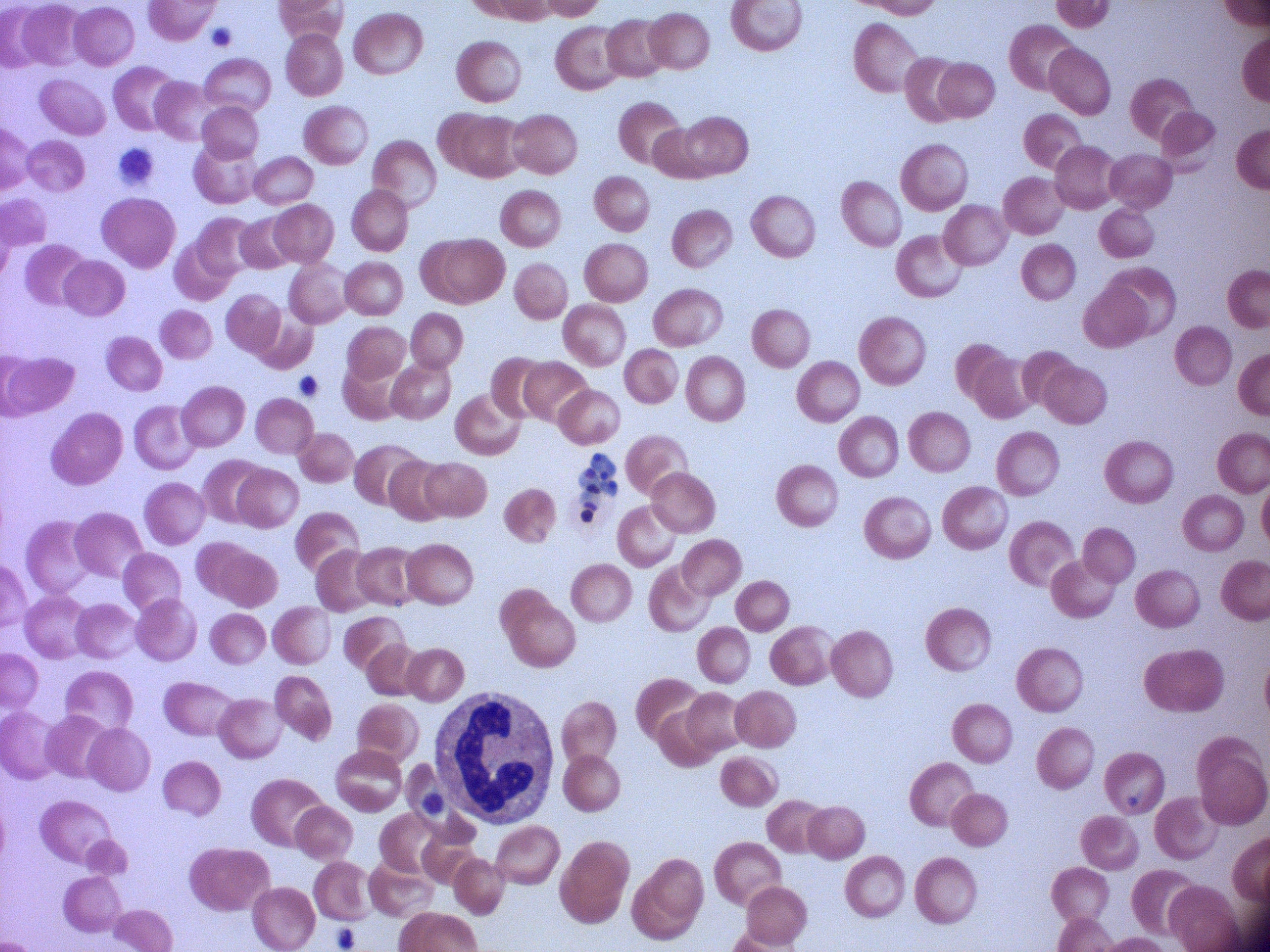
preparation = thin blood smear
magnification = 100x
schizont locations = approximate bounding boxes as (x1,y1)-(x2,y2) corner pairs in pixels, from the source annotation, which is not necessarily exhaustive: (579,453)-(618,523)
image size = 1270×952 pixels
species = Plasmodium falciparum
stain = Giemsa
microscope = Leica DM2000 with built-in camera
field of view = single